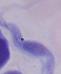
Summary:
  - Modality: micrograph
  - Magnification: 1000x
  - Identification: trypanosome